Assess this cell for malaria.
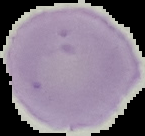

Uninfected.

Segmented cell region on a black background. Image is 145×136 pixels. From a thin blood smear.